Report the malaria status of this cell.
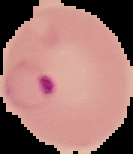
Parasitized.

Summary:
  - Preparation: thin blood film
  - Image size: 133×154 pixels
  - Image type: segmented cell region on a black background